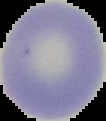 Cell region segmented out of the field of view; the surrounding area is masked to black. Malaria status: uninfected. From a thin blood film. Image is 106×121 pixels.